Classify this cell by malaria status.
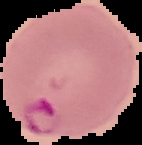

Parasitized.

preparation = thin blood film
image size = 142×145 pixels
image type = segmented cell region with the area outside set to black